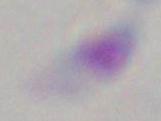
Summary:
  - Modality: micrograph
  - Identification: Toxoplasma gondii
  - Magnification: 1000x